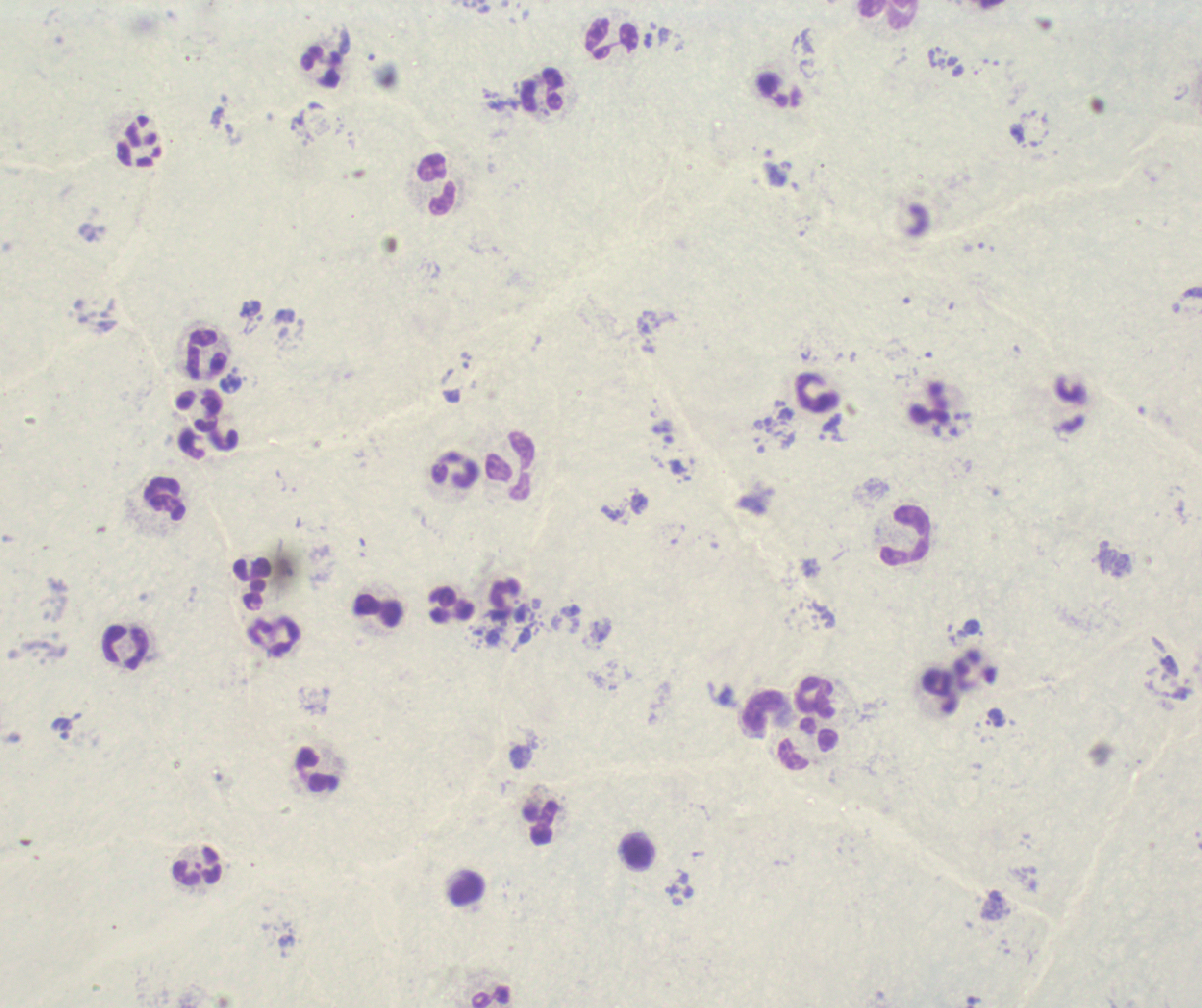
Approximate centers as (x, y) in pixels.
Summary:
  - Leukocyte locations: (886, 13), (611, 38), (321, 68), (542, 89), (437, 183), (207, 353), (817, 394), (930, 403), (510, 467), (456, 470), (164, 498), (905, 536), (252, 584), (451, 605), (379, 611), (126, 648), (816, 698), (763, 712), (807, 745), (317, 769), (540, 823), (638, 850), (198, 865)
  - Result: negative for Plasmodium parasites
  - Preparation: thick smear of blood
  - Field of view: one from this slide
  - Magnification: 100x
  - Context: previously used in a real diagnosis
  - Image size: 1202×1008 pixels
  - Stain: Romanowsky
  - Background quality: poor